Give the extent of all Plasmodium falciparum-infected red blood cells.
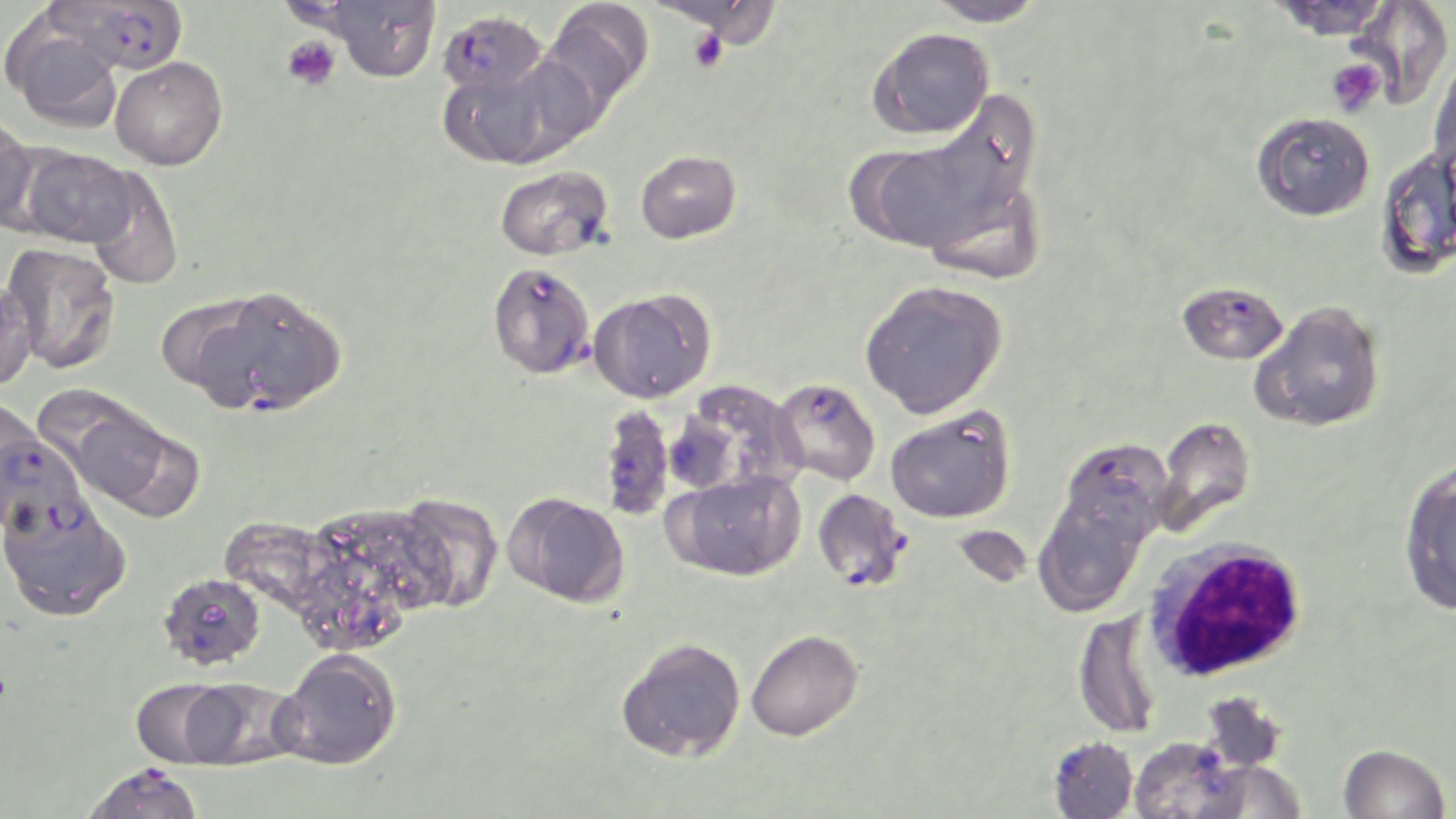
Approximate bounding boxes as named x1/y1/x2/y2 corners in pixels.
Plasmodium falciparum-infected red blood cells: (x1=50, y1=0, x2=189, y2=74), (x1=438, y1=10, x2=548, y2=100), (x1=494, y1=266, x2=597, y2=382), (x1=1176, y1=280, x2=1289, y2=365), (x1=770, y1=377, x2=881, y2=486), (x1=596, y1=403, x2=675, y2=522), (x1=0, y1=425, x2=90, y2=539), (x1=1057, y1=437, x2=1174, y2=554), (x1=812, y1=489, x2=910, y2=592), (x1=80, y1=763, x2=205, y2=819).

Summary:
  - Platelet locations: (x1=688, y1=28, x2=729, y2=73), (x1=281, y1=36, x2=340, y2=91), (x1=1326, y1=60, x2=1385, y2=116)
  - White blood cell locations: (x1=1143, y1=536, x2=1309, y2=683)
  - Uninfected red blood cell locations: (x1=321, y1=0, x2=442, y2=81), (x1=542, y1=0, x2=655, y2=107), (x1=922, y1=0, x2=1047, y2=27), (x1=1267, y1=0, x2=1395, y2=40), (x1=1344, y1=0, x2=1454, y2=110), (x1=3, y1=13, x2=125, y2=132), (x1=867, y1=27, x2=994, y2=139), (x1=1430, y1=51, x2=1456, y2=177), (x1=437, y1=52, x2=584, y2=169), (x1=110, y1=56, x2=228, y2=170), (x1=849, y1=97, x2=1043, y2=263), (x1=1252, y1=111, x2=1375, y2=222), (x1=0, y1=113, x2=39, y2=233), (x1=1376, y1=145, x2=1456, y2=281), (x1=18, y1=147, x2=136, y2=248), (x1=635, y1=150, x2=742, y2=244), (x1=494, y1=166, x2=614, y2=261), (x1=82, y1=167, x2=185, y2=290), (x1=1, y1=242, x2=121, y2=375), (x1=0, y1=276, x2=38, y2=391), (x1=859, y1=279, x2=1008, y2=419), (x1=190, y1=285, x2=346, y2=418), (x1=587, y1=287, x2=715, y2=404), (x1=1250, y1=301, x2=1385, y2=433), (x1=670, y1=381, x2=801, y2=497), (x1=54, y1=400, x2=201, y2=518), (x1=885, y1=407, x2=1015, y2=523), (x1=1152, y1=416, x2=1255, y2=537), (x1=1398, y1=463, x2=1456, y2=616), (x1=667, y1=470, x2=805, y2=582), (x1=502, y1=491, x2=629, y2=607), (x1=1033, y1=492, x2=1150, y2=617), (x1=391, y1=493, x2=504, y2=614), (x1=0, y1=495, x2=131, y2=623), (x1=289, y1=501, x2=449, y2=653), (x1=158, y1=571, x2=266, y2=669), (x1=1073, y1=610, x2=1162, y2=740), (x1=745, y1=629, x2=863, y2=742), (x1=616, y1=637, x2=746, y2=763), (x1=274, y1=648, x2=403, y2=770), (x1=130, y1=678, x2=238, y2=768), (x1=178, y1=678, x2=298, y2=769), (x1=1048, y1=736, x2=1138, y2=819), (x1=1129, y1=737, x2=1244, y2=819), (x1=1338, y1=743, x2=1450, y2=819)
  - Slide-level diagnosis: Plasmodium falciparum
  - Magnification: 1000x
  - Modality: light microscopy
  - Preparation: thin blood film
  - Field of view: single
  - Stain: May-Grünwald-Giemsa
  - Image size: 1456×819 pixels